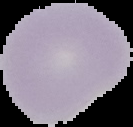

Segmented cell region on a black background. Result: negative for malaria parasites. Image is 133×127 pixels. From a thin blood smear.